Name the parasite shown.
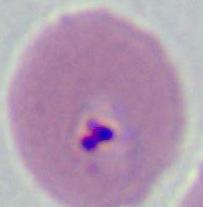

Plasmodium.

Summary:
  - Modality: photomicrograph
  - Magnification: 400x or 1000x